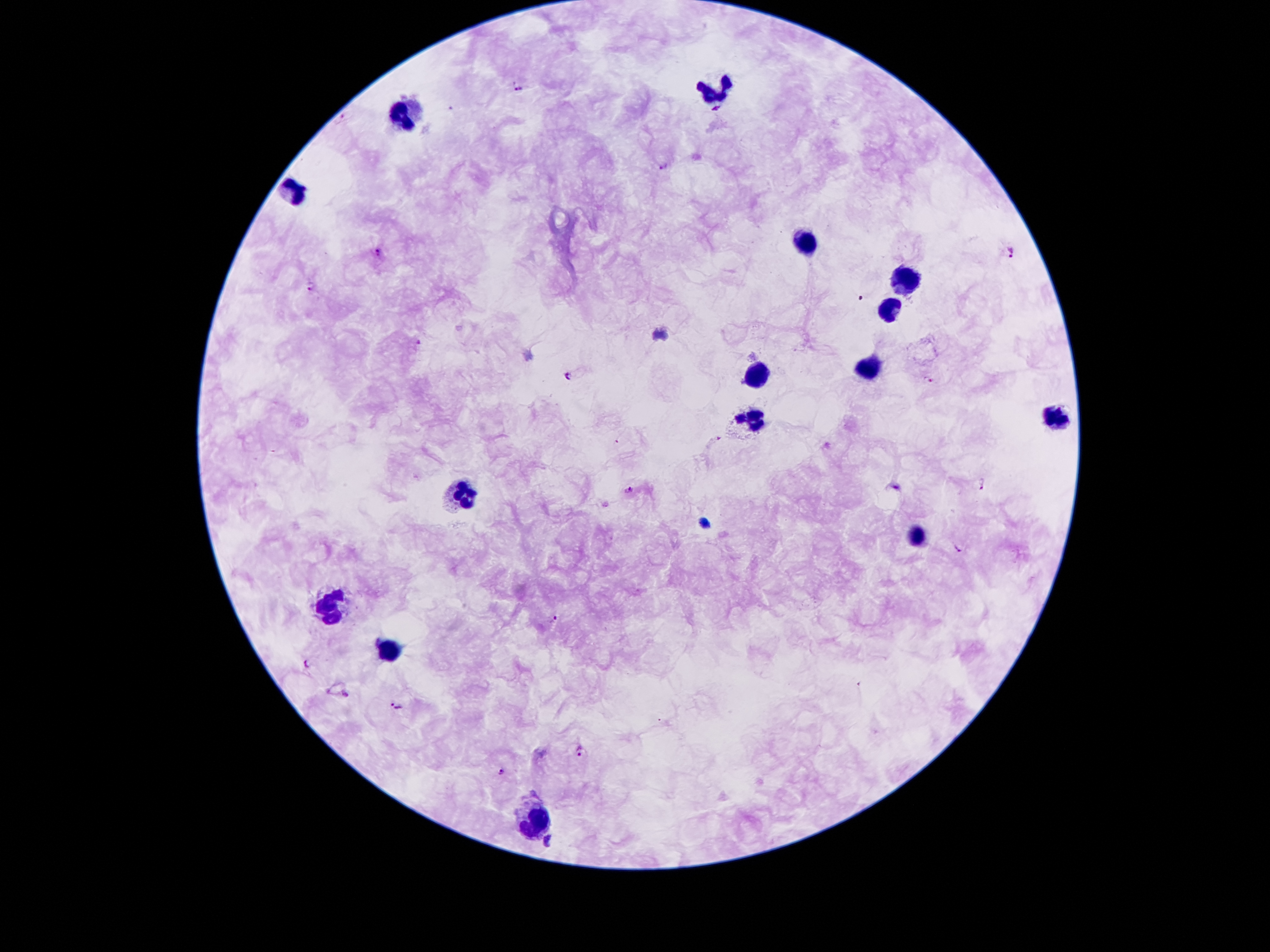
Approximate centers as [x, y] in pixels.
Summary:
  - Leukocyte locations: [717, 91], [406, 118], [295, 191], [809, 245], [905, 276], [885, 307], [863, 369], [754, 374], [1058, 418], [747, 421], [463, 493], [917, 535], [329, 608], [391, 651], [534, 819]
  - Malaria parasite locations: [519, 89], [450, 108], [342, 116], [665, 167], [1010, 252], [380, 253], [311, 286], [418, 341], [567, 376], [932, 381], [984, 484], [630, 491], [958, 549], [556, 620], [307, 662], [397, 706], [582, 750], [501, 771], [547, 842]
  - Preparation: thick peripheral-blood smear
  - Field of view: one from this slide
  - Patient malaria status: positive for Plasmodium falciparum
  - Image size: 1270×952 pixels
  - Stain: Giemsa
  - Magnification: 100x
  - Capture: smartphone camera through the microscope eyepiece